Classify this cell by malaria status.
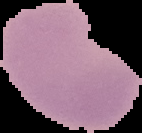
It is uninfected.

From a thin blood smear. Image is 142×133 pixels. Segmented cell region on a black background.